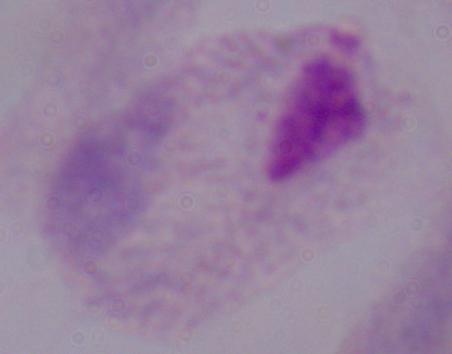

magnification = 1000x
modality = micrograph
identification = trichomonad